Locate every uninfected red blood cell.
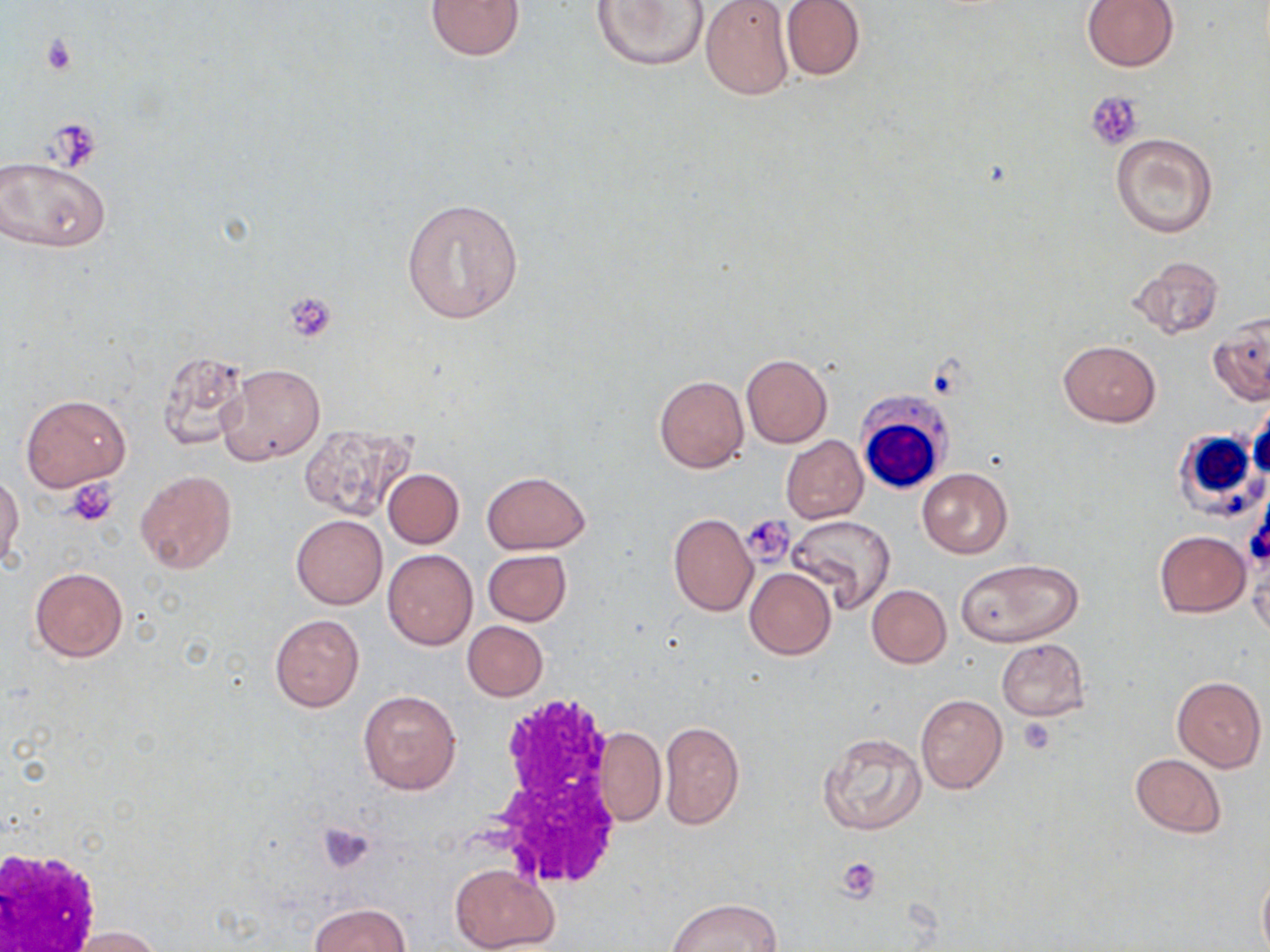

Approximate bounding boxes as (x1, y1, x2, y2) in pixels.
Uninfected red blood cells: (425, 0, 526, 61), (591, 0, 710, 71), (699, 0, 794, 101), (780, 0, 866, 82), (1082, 0, 1179, 73), (1111, 133, 1218, 238), (0, 153, 112, 254), (402, 197, 524, 324), (1128, 255, 1225, 340), (1209, 315, 1270, 406), (1058, 341, 1161, 426), (154, 353, 252, 451), (741, 354, 833, 448), (218, 362, 325, 464), (654, 375, 748, 473), (21, 395, 130, 491), (300, 425, 419, 528), (781, 435, 868, 524), (917, 467, 1012, 558), (383, 468, 464, 548), (135, 470, 235, 573), (482, 471, 590, 553), (0, 472, 24, 570), (291, 514, 387, 609), (668, 514, 758, 616), (785, 514, 895, 612), (1154, 530, 1252, 618), (383, 548, 477, 650), (483, 548, 571, 626), (1248, 549, 1269, 640), (957, 558, 1084, 646), (30, 567, 129, 661), (745, 568, 835, 660), (867, 585, 951, 667), (270, 614, 364, 712), (462, 621, 547, 701), (995, 638, 1090, 720), (1171, 675, 1266, 771), (357, 689, 461, 795), (915, 693, 1007, 793), (659, 720, 745, 830), (593, 727, 666, 826), (817, 730, 927, 836), (1129, 753, 1226, 838), (450, 863, 558, 952), (1257, 870, 1270, 951), (668, 898, 781, 951), (309, 903, 409, 952), (63, 927, 166, 952).

White blood cell locations: (856, 392, 952, 494), (1170, 429, 1265, 519), (481, 697, 615, 887), (1, 845, 105, 952). Platelet locations: (39, 34, 78, 75), (1086, 93, 1144, 150), (40, 122, 96, 170), (284, 291, 338, 342), (63, 477, 117, 527), (740, 516, 793, 566), (1017, 719, 1055, 755), (319, 821, 376, 874), (837, 857, 881, 902). Slide-level diagnosis: no evidence of blood parasites. May-Grünwald-Giemsa stain. One field of a larger specimen. Optical microscopy. Thin blood smear. Captured at 1000x magnification. Image is 1270×952 pixels.